Comment on the morphology of the erythrocytes.
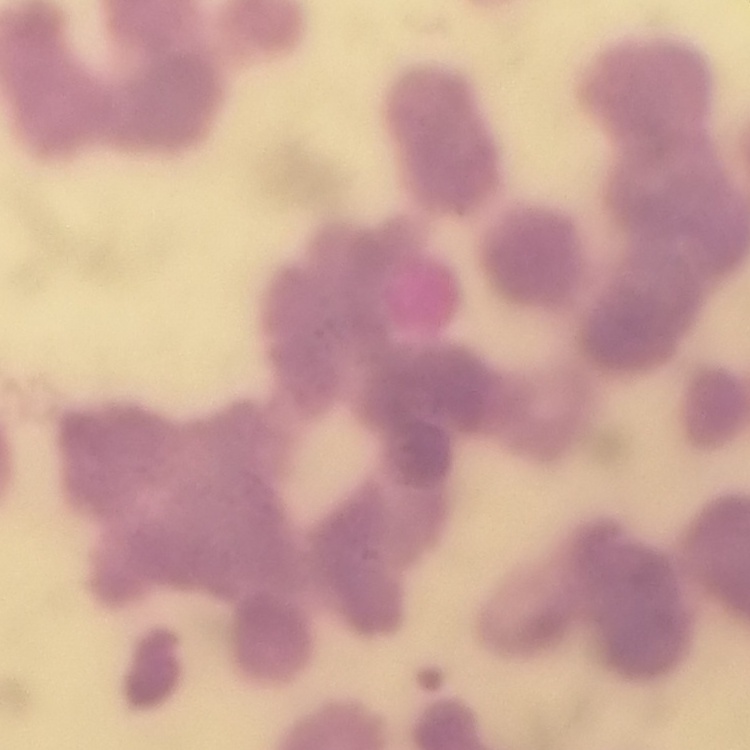
Rouleaux formation.

Thin blood smear. Stained with either Field's or Giemsa. Square crop of a larger photomicrograph.